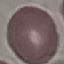

result = no malaria parasites seen
preparation = thin blood film
image type = cell patch, automatically extracted from a larger field of view and resized to 64 × 64 pixels
stain = Giemsa
capture = smartphone through the microscope eyepiece